Comment on the morphology of the erythrocytes.
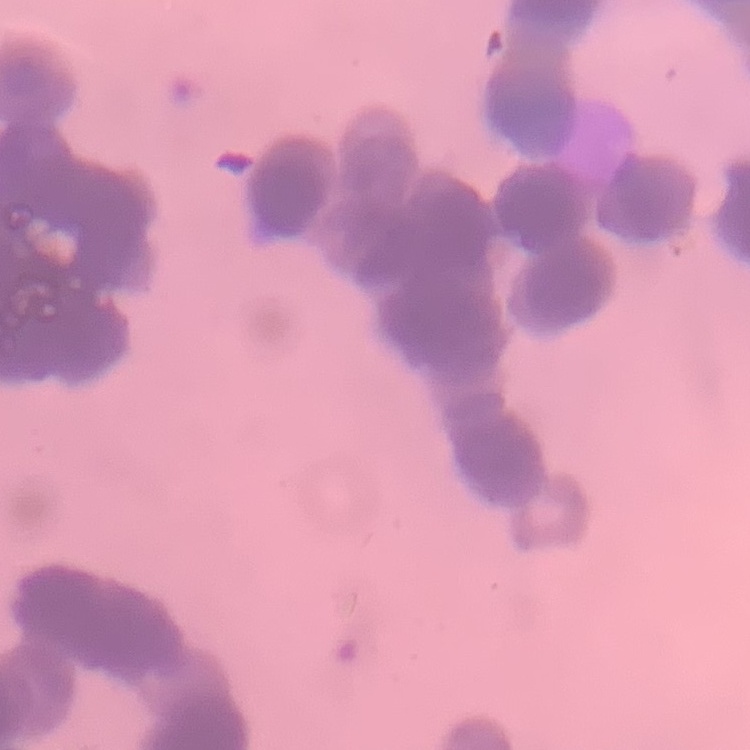

They show rouleaux formation.

Summary:
  - Image type: square crop of a larger photomicrograph
  - Stain: Field's or Giemsa
  - Preparation: thin blood smear